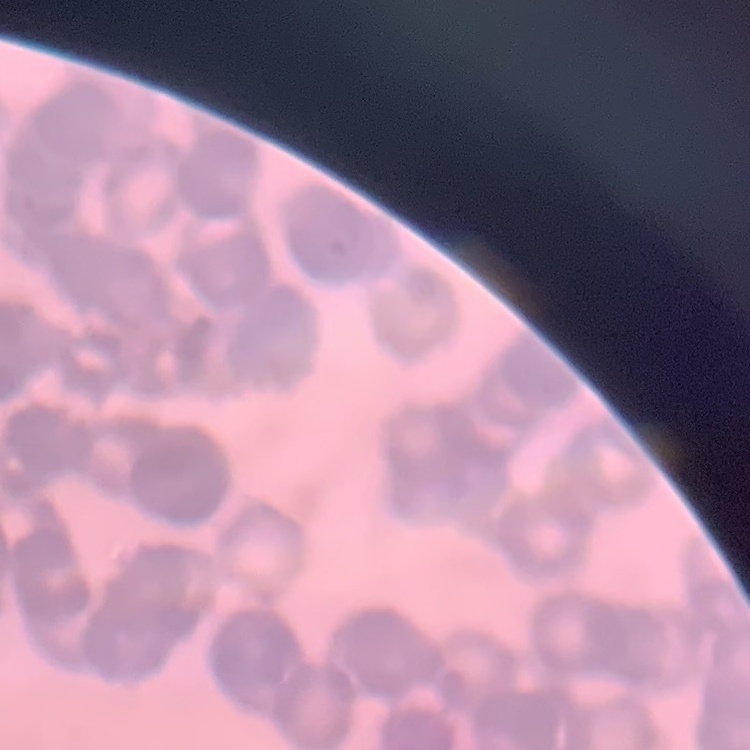
erythrocyte morphology = rouleaux formation
image type = one tile cut from a larger photomicrograph
preparation = thin blood smear
stain = Field's or Giemsa